Report the malaria status of this cell.
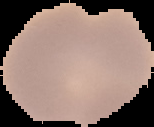

Uninfected.

Summary:
  - Preparation: thin blood film
  - Image size: 154×127 pixels
  - Image type: cell region segmented out of the field of view; surrounding area masked to black